Classify this cell by malaria status.
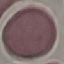
It is uninfected.

Summary:
  - Capture: smartphone camera at the microscope eyepiece
  - Stain: Giemsa
  - Image type: cell patch, automatically extracted from a larger field of view and resized to 64 × 64 pixels
  - Preparation: thin blood smear